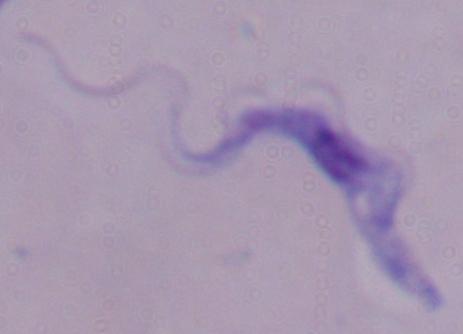
Summary:
  - Identification: trypanosome
  - Modality: photomicrograph
  - Magnification: 1000x